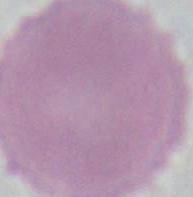

Captured at 1000x magnification. A red blood cell is seen. Micrograph.